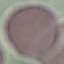
malaria_status: uninfected
capture: smartphone camera at the microscope eyepiece
preparation: thin smear
image_type: automatically extracted cell patch, resized to 64 × 64 pixels
stain: Giemsa